Locate every blood parasite and identify its species.
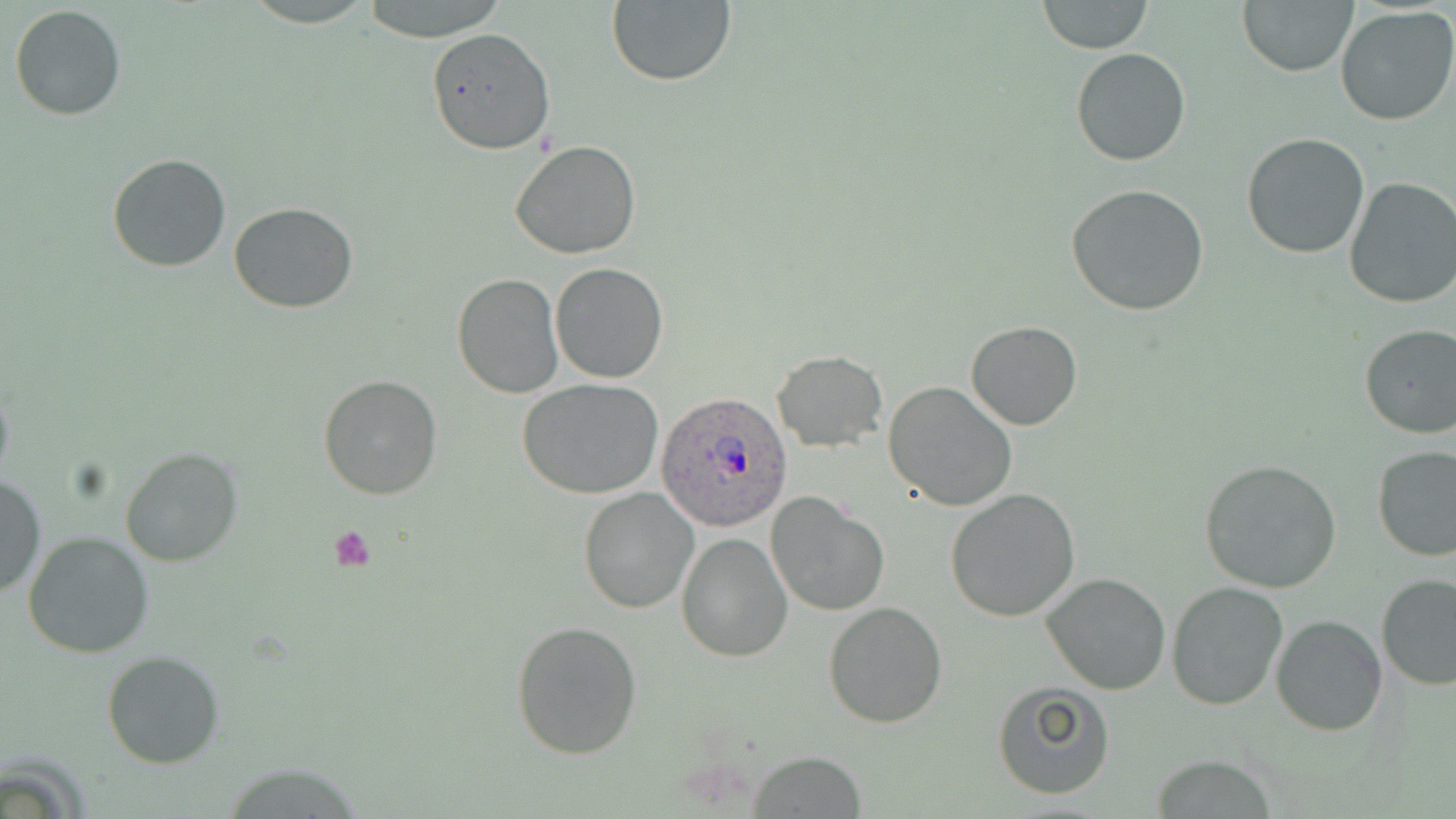
Approximate bounding boxes as (x1, y1, x2, y2) in pixels.
Plasmodium ovale-infected red blood cells: (655, 393, 796, 533).
No Plasmodium falciparum, Plasmodium malariae, Plasmodium vivax, Babesia divergens, or Trypanosoma brucei observed.

Uninfected red blood cell locations: (357, 0, 512, 43), (1238, 0, 1357, 77), (606, 1, 736, 87), (1038, 1, 1152, 54), (9, 4, 126, 120), (1335, 7, 1456, 126), (426, 27, 554, 155), (1071, 47, 1191, 167), (1241, 133, 1370, 259), (509, 140, 642, 260), (107, 154, 232, 273), (1344, 176, 1456, 308), (1066, 184, 1210, 317), (229, 202, 359, 313), (550, 263, 669, 383), (452, 272, 564, 397), (967, 322, 1081, 431), (1357, 323, 1456, 440), (773, 350, 887, 452), (319, 374, 442, 500), (0, 375, 15, 492), (516, 378, 664, 499), (883, 380, 1018, 513), (1373, 446, 1456, 561), (120, 447, 243, 568), (1199, 459, 1343, 594), (0, 472, 44, 601), (579, 487, 701, 614), (944, 488, 1080, 622), (765, 491, 889, 617), (23, 530, 154, 659), (675, 532, 793, 663), (1041, 571, 1170, 696), (1376, 574, 1456, 691), (1167, 582, 1289, 712), (822, 601, 948, 729), (1271, 614, 1389, 736), (510, 620, 643, 760), (101, 650, 225, 769), (991, 682, 1116, 800), (751, 751, 867, 817), (1150, 757, 1282, 817). Platelet locations: (327, 525, 378, 573). Slide-level diagnosis: Plasmodium ovale. Thin blood film. Light microscopy. One field of a larger specimen. May-Grünwald-Giemsa stain. Image is 1456×819 pixels. Captured at 1000x magnification.